Report the malaria status of this cell.
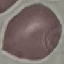
It is uninfected.

stain = Giemsa
preparation = thin smear
image type = cell patch, automatically extracted from a larger field of view and resized to 64 × 64 pixels
capture = smartphone through the microscope eyepiece